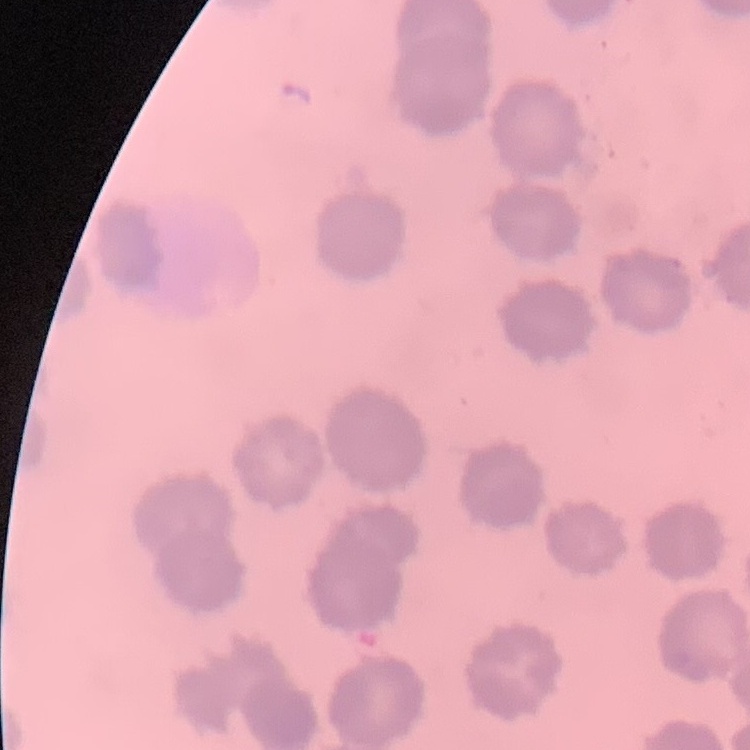
{
  "erythrocyte_morphology": "no rouleaux formation",
  "preparation": "thin blood smear",
  "image_type": "square crop of a larger photomicrograph",
  "stain": "Field's or Giemsa"
}